Locate every blood parasite and identify its species.
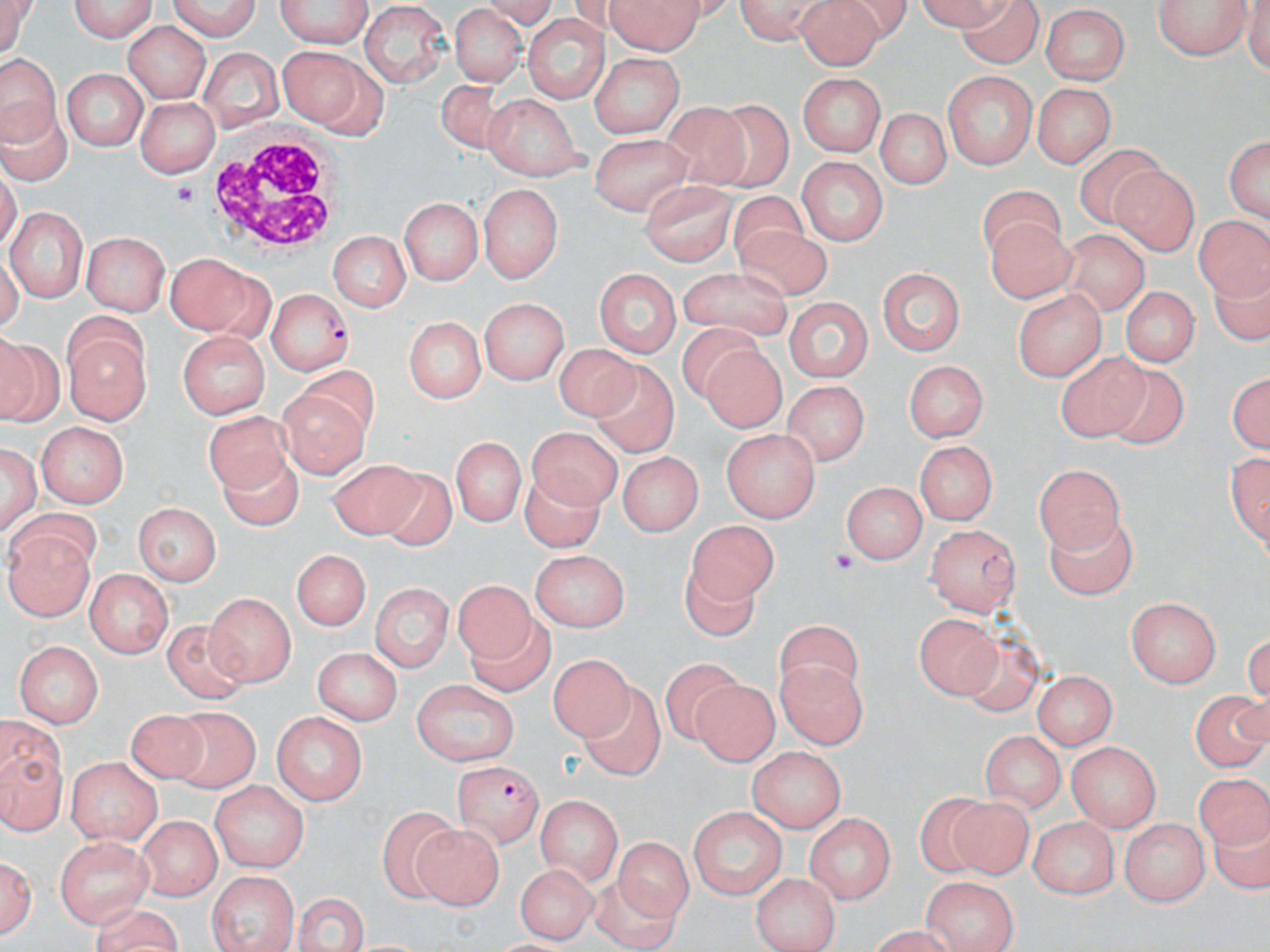
Approximate bounding boxes as (x1,y1)-(x2,y2) corner pairs in pixels.
Plasmodium falciparum-infected red blood cells: (264,289)-(355,373), (455,762)-(543,847).
No Plasmodium ovale, Plasmodium malariae, Plasmodium vivax, Babesia divergens, or Trypanosoma brucei observed.

Summary:
  - White blood cell locations: (205,133)-(344,255)
  - Platelet locations: (169,184)-(198,211), (831,550)-(856,573)
  - Uninfected red blood cell locations: (1,0)-(37,58), (67,0)-(160,38), (162,0)-(262,38), (277,0)-(376,51), (606,0)-(713,54), (731,0)-(828,40), (956,0)-(1041,69), (1153,0)-(1249,60), (794,1)-(881,70), (452,4)-(526,89), (1038,6)-(1132,83), (357,7)-(451,85), (521,14)-(605,105), (125,18)-(209,102), (277,44)-(374,133), (197,45)-(281,134), (592,52)-(684,137), (2,56)-(57,149), (59,66)-(148,151), (942,71)-(1037,169), (799,72)-(887,159), (434,78)-(522,162), (1035,80)-(1117,166), (487,93)-(580,181), (136,98)-(221,175), (707,100)-(796,187), (654,101)-(753,192), (872,107)-(953,191), (1223,131)-(1269,228), (588,132)-(694,212), (1074,142)-(1163,223), (796,158)-(884,248), (1107,163)-(1198,253), (641,181)-(736,262), (479,182)-(560,285), (978,186)-(1063,261), (727,190)-(808,266), (397,199)-(483,285), (12,208)-(85,302), (981,214)-(1072,303), (1194,215)-(1270,304), (734,226)-(830,302), (325,231)-(412,312), (1058,231)-(1146,316), (84,232)-(171,317), (165,251)-(258,335), (876,262)-(964,357), (680,265)-(796,339), (595,269)-(681,360), (1119,286)-(1199,368), (1012,288)-(1110,380), (783,295)-(875,383), (479,297)-(571,386), (405,314)-(484,403), (678,325)-(764,404), (176,328)-(275,420), (65,332)-(149,422), (0,334)-(51,428), (701,345)-(792,434), (552,346)-(644,425), (1056,351)-(1152,444), (589,358)-(674,458), (901,359)-(988,444), (1095,366)-(1186,448), (1226,366)-(1268,453), (302,368)-(387,444), (784,379)-(867,468), (271,389)-(367,484), (202,413)-(294,500), (37,422)-(132,508), (529,426)-(624,512), (723,430)-(820,522), (452,433)-(525,526), (2,440)-(41,533), (913,440)-(998,526), (216,446)-(302,533), (615,450)-(703,536), (326,459)-(430,540), (1031,460)-(1130,544), (517,463)-(604,552), (373,467)-(464,551), (841,477)-(926,566), (135,502)-(221,584), (1045,510)-(1134,602), (6,520)-(99,618), (106,520)-(221,614), (687,522)-(776,607), (927,522)-(1021,615), (292,548)-(372,635), (527,550)-(631,630), (681,564)-(760,641), (85,569)-(174,658), (371,580)-(452,673), (452,581)-(539,666), (204,591)-(292,686), (1127,597)-(1223,687), (469,610)-(559,699), (918,614)-(1006,703), (161,621)-(256,705), (775,623)-(861,703), (960,633)-(1041,717), (11,639)-(101,726), (310,646)-(405,723), (545,649)-(636,739), (780,657)-(870,745), (662,660)-(744,744), (1032,669)-(1116,750), (413,677)-(519,766), (692,678)-(779,769), (584,684)-(665,784), (1193,685)-(1268,767), (126,704)-(205,786), (170,707)-(258,794), (272,709)-(369,805), (2,718)-(69,838), (979,729)-(1065,813), (1065,739)-(1161,833), (749,747)-(845,836), (66,754)-(162,844), (1193,769)-(1267,848), (209,781)-(311,870), (537,793)-(622,883), (915,794)-(993,874), (945,798)-(1035,875), (376,806)-(464,901), (688,807)-(787,902), (803,811)-(900,901), (1027,813)-(1122,897), (136,815)-(222,898), (1122,818)-(1209,904), (411,825)-(502,909), (54,833)-(152,931), (613,839)-(703,921), (2,848)-(38,940), (508,862)-(595,940), (207,872)-(301,952), (752,872)-(843,952), (924,874)-(1022,947), (589,875)-(683,948), (291,891)-(370,952)
  - Slide-level diagnosis: Plasmodium falciparum
  - Magnification: 1000x
  - Preparation: thin blood smear
  - Image size: 1270×952 pixels
  - Modality: light microscopy
  - Field of view: one of a larger specimen
  - Stain: May-Grünwald-Giemsa